Classify this cell by malaria status.
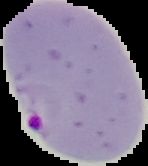

Parasitized.

Summary:
  - Preparation: thin blood film
  - Image size: 148×166 pixels
  - Image type: segmented cell region with the area outside set to black